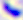
identification = Toxoplasma gondii
magnification = 400x
modality = micrograph